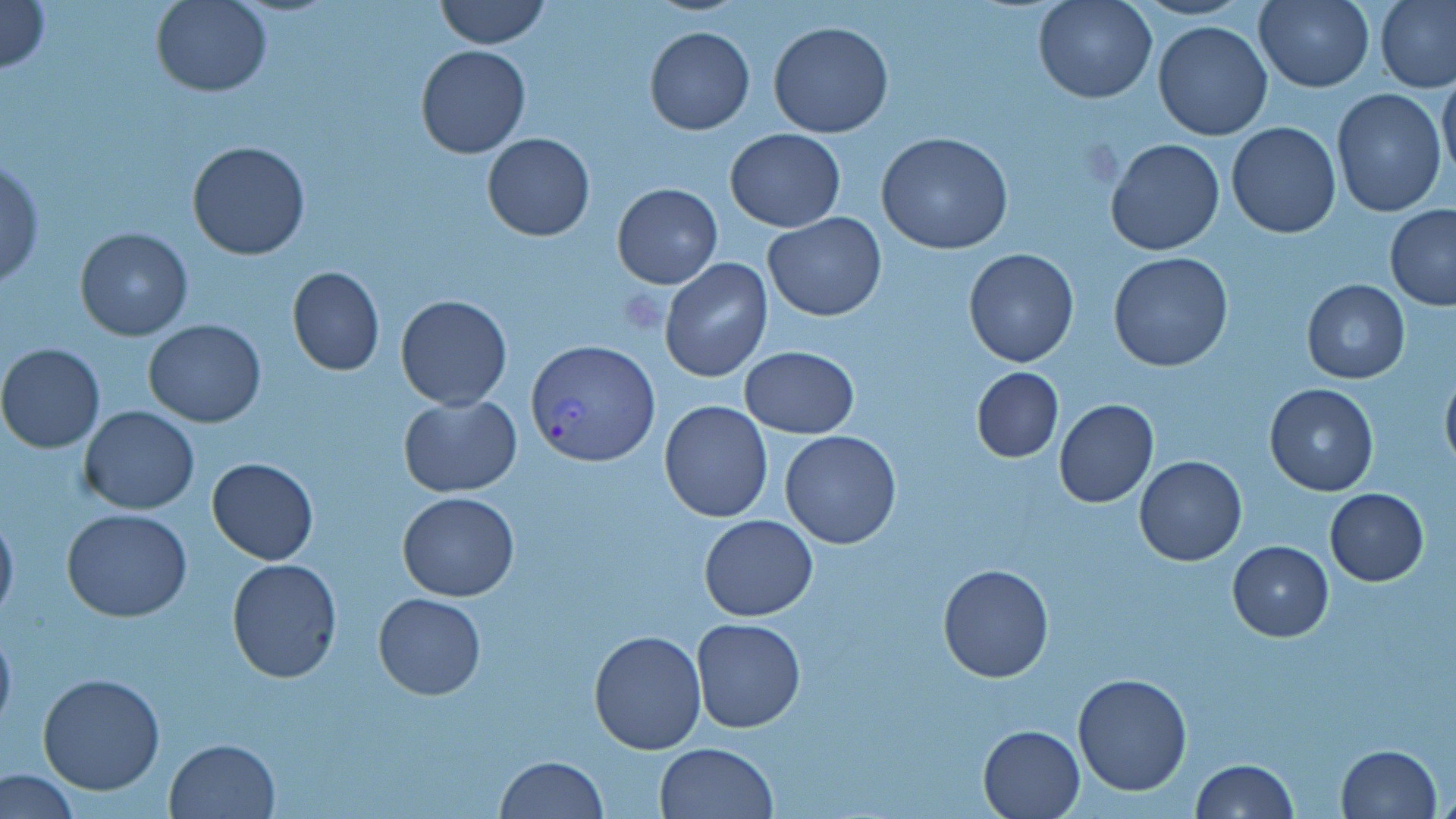

Approximate bounding boxes as [x1, y1, x2, y2] in pixels. Plasmodium vivax-infected red blood cell locations: [525, 339, 660, 466]. Uninfected red blood cell locations: [0, 0, 50, 76], [151, 0, 273, 97], [435, 0, 548, 48], [1033, 0, 1158, 104], [1252, 0, 1374, 92], [1376, 0, 1456, 94], [768, 20, 893, 137], [1152, 20, 1273, 140], [644, 26, 755, 135], [416, 44, 530, 158], [1439, 67, 1456, 181], [1332, 87, 1447, 216], [1225, 110, 1446, 225], [1225, 121, 1342, 238], [725, 130, 847, 232], [876, 132, 1015, 256], [482, 133, 595, 241], [1104, 136, 1226, 257], [187, 140, 312, 261], [1, 157, 45, 292], [612, 182, 723, 288], [1385, 205, 1456, 310], [763, 213, 887, 323], [75, 228, 194, 341], [964, 247, 1079, 367], [1108, 252, 1234, 373], [660, 259, 774, 383], [286, 266, 384, 377], [1302, 280, 1410, 384], [393, 293, 514, 410], [143, 319, 266, 428], [1, 343, 105, 453], [740, 345, 857, 439], [971, 366, 1063, 463], [1440, 366, 1456, 478], [1265, 382, 1378, 495], [397, 395, 522, 497], [1054, 399, 1158, 507], [659, 401, 774, 521], [79, 406, 200, 514], [779, 430, 903, 549], [1134, 455, 1247, 567], [207, 456, 318, 565], [1325, 488, 1429, 585], [397, 492, 521, 602], [0, 507, 18, 627], [63, 508, 193, 622], [699, 515, 819, 620], [1228, 539, 1333, 640], [226, 558, 342, 682], [938, 564, 1054, 683], [373, 592, 486, 699], [690, 618, 808, 734], [0, 621, 17, 738], [588, 628, 706, 753], [38, 672, 166, 794], [1072, 672, 1193, 795], [978, 723, 1087, 818], [164, 736, 282, 819], [656, 741, 779, 819], [1335, 744, 1441, 819], [496, 756, 608, 818], [1190, 759, 1297, 818], [1, 768, 80, 818]. Platelet locations: [619, 291, 666, 334]. Slide-level diagnosis: Plasmodium vivax. Captured at 1000x magnification. Thin blood film. Light microscopy. May-Grünwald-Giemsa-stained preparation. Image is 1456×819 pixels. One field of a larger specimen.